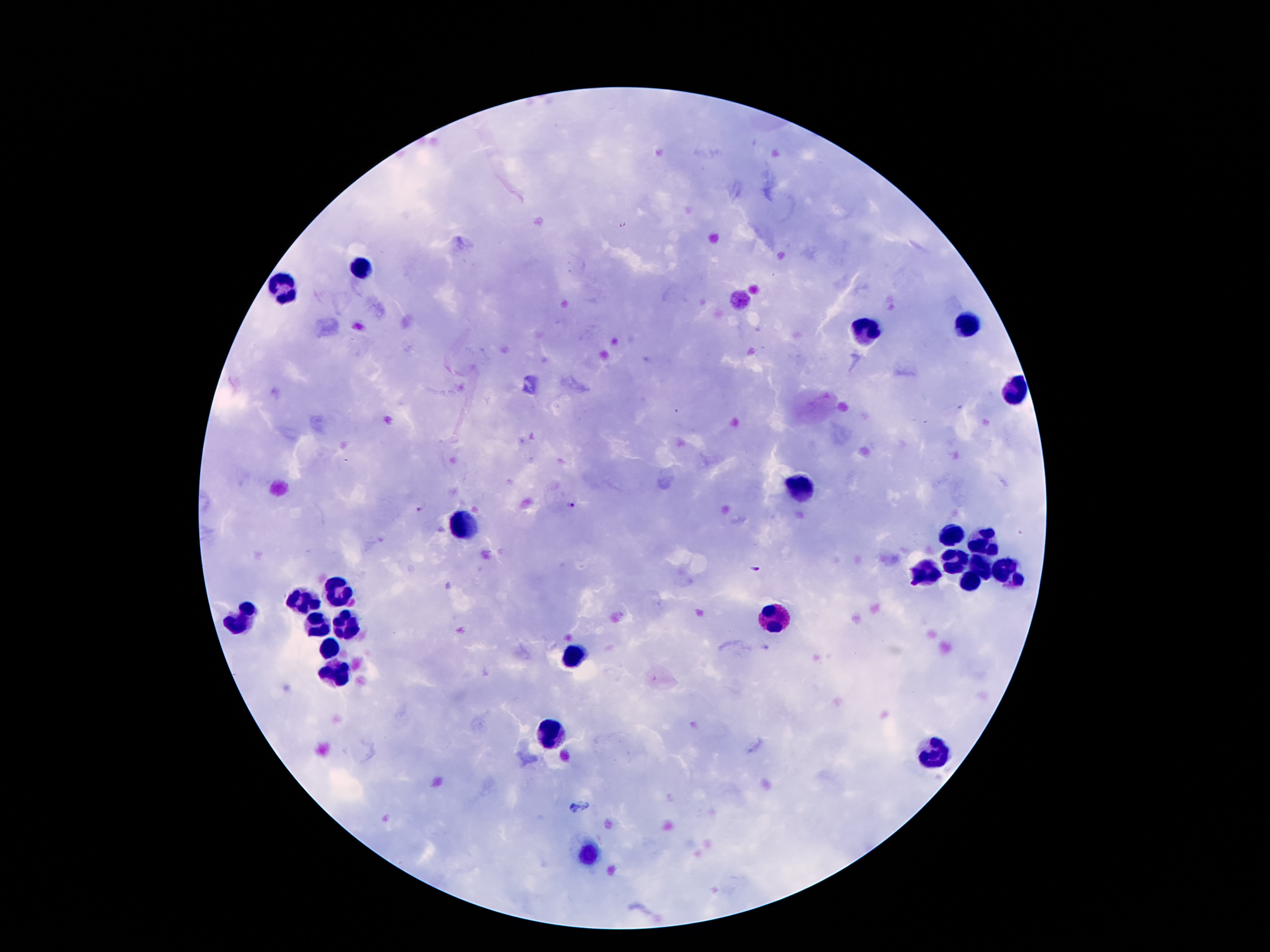
Approximate object centers, in pixels from the top-left corner.
Summary:
  - Leukocyte locations: (x=968, y=324), (x=863, y=332), (x=1017, y=392), (x=799, y=483), (x=462, y=527), (x=951, y=535), (x=984, y=542), (x=954, y=564), (x=981, y=565), (x=1007, y=572), (x=922, y=577), (x=973, y=584), (x=339, y=592), (x=301, y=606), (x=244, y=616), (x=778, y=616), (x=346, y=623), (x=318, y=625), (x=332, y=646), (x=574, y=655), (x=339, y=671), (x=555, y=730), (x=938, y=757), (x=590, y=857)
  - Plasmodium parasite locations: (x=571, y=504), (x=420, y=509), (x=755, y=569)
  - Preparation: thick blood film
  - Patient malaria status: infected with Plasmodium falciparum
  - Capture: smartphone through the microscope eyepiece
  - Stain: Giemsa
  - Magnification: 100x
  - Field of view: one from this slide
  - Image size: 1270×952 pixels